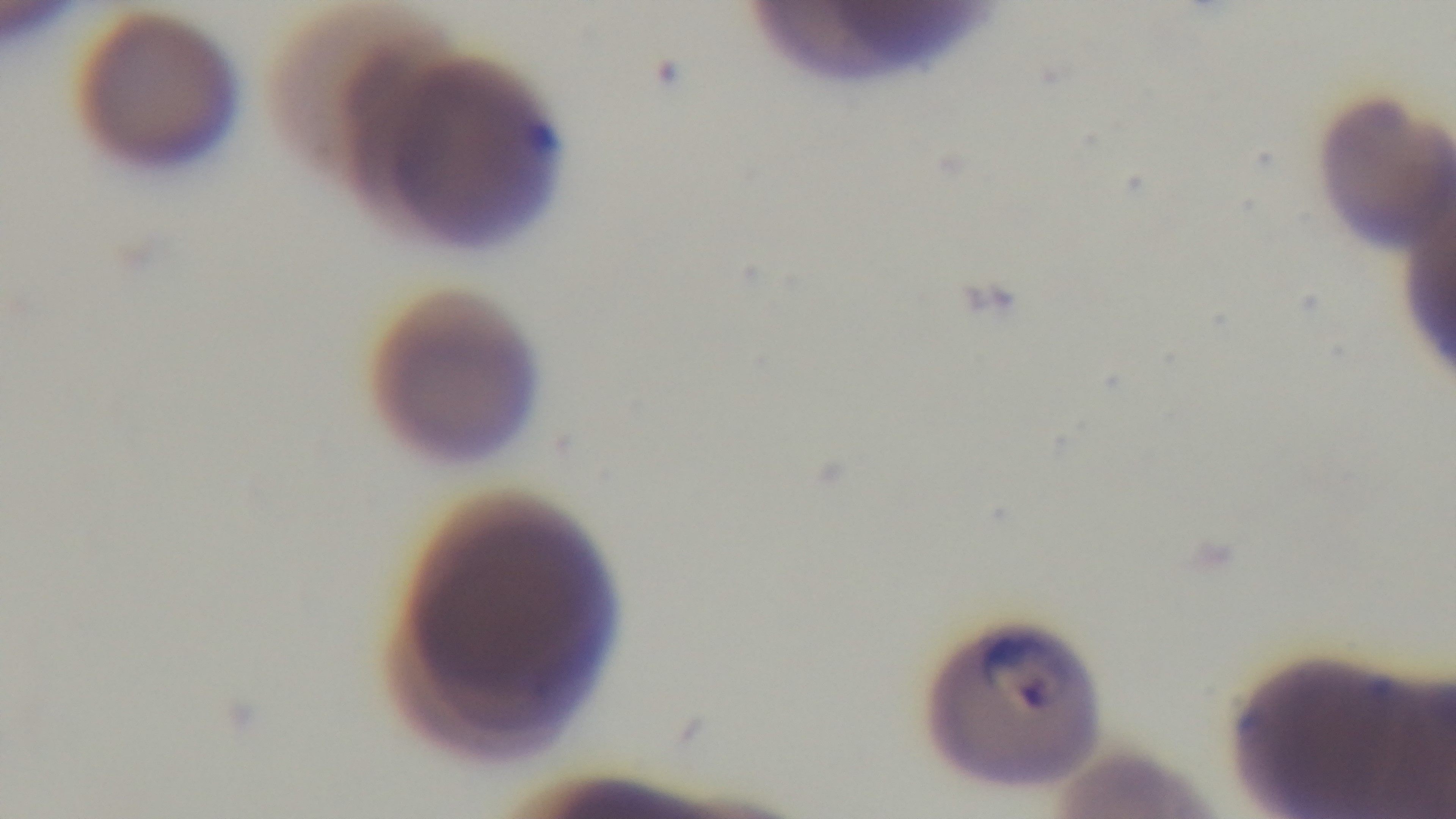

Summary:
  - Modality: light microscopy
  - Capture: mounted 4K digital camera
  - Malaria status: positive
  - Field of view: single
  - Stain: Giemsa
  - Preparation: thin smear
  - Objective: 100x oil immersion